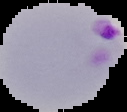

Summary:
  - Malaria status: parasitized
  - Image type: segmented cell region with the area outside set to black
  - Preparation: thin blood film
  - Image size: 127×112 pixels